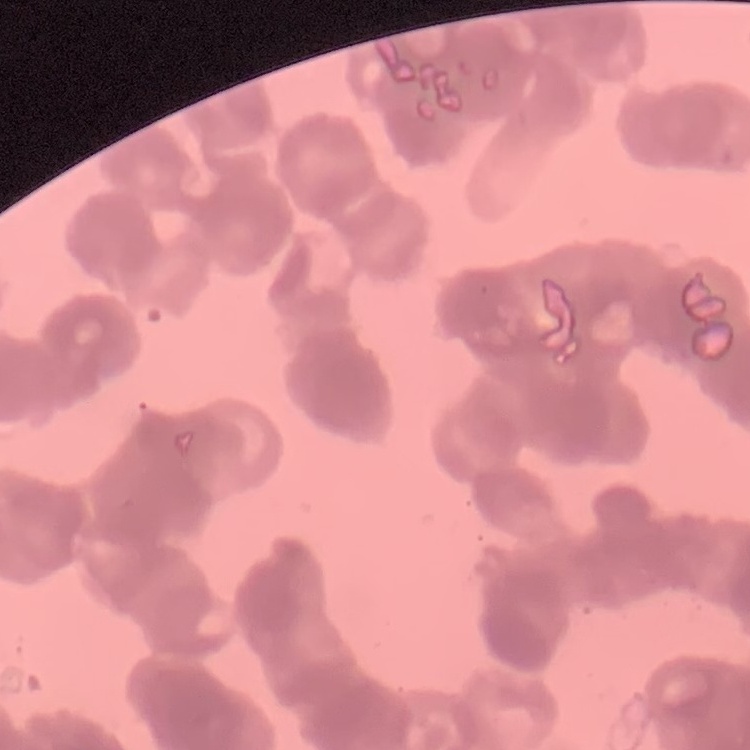
red blood cell morphology = rouleaux formation
preparation = thin blood smear
stain = Field's or Giemsa
image type = one tile cut from a larger photomicrograph